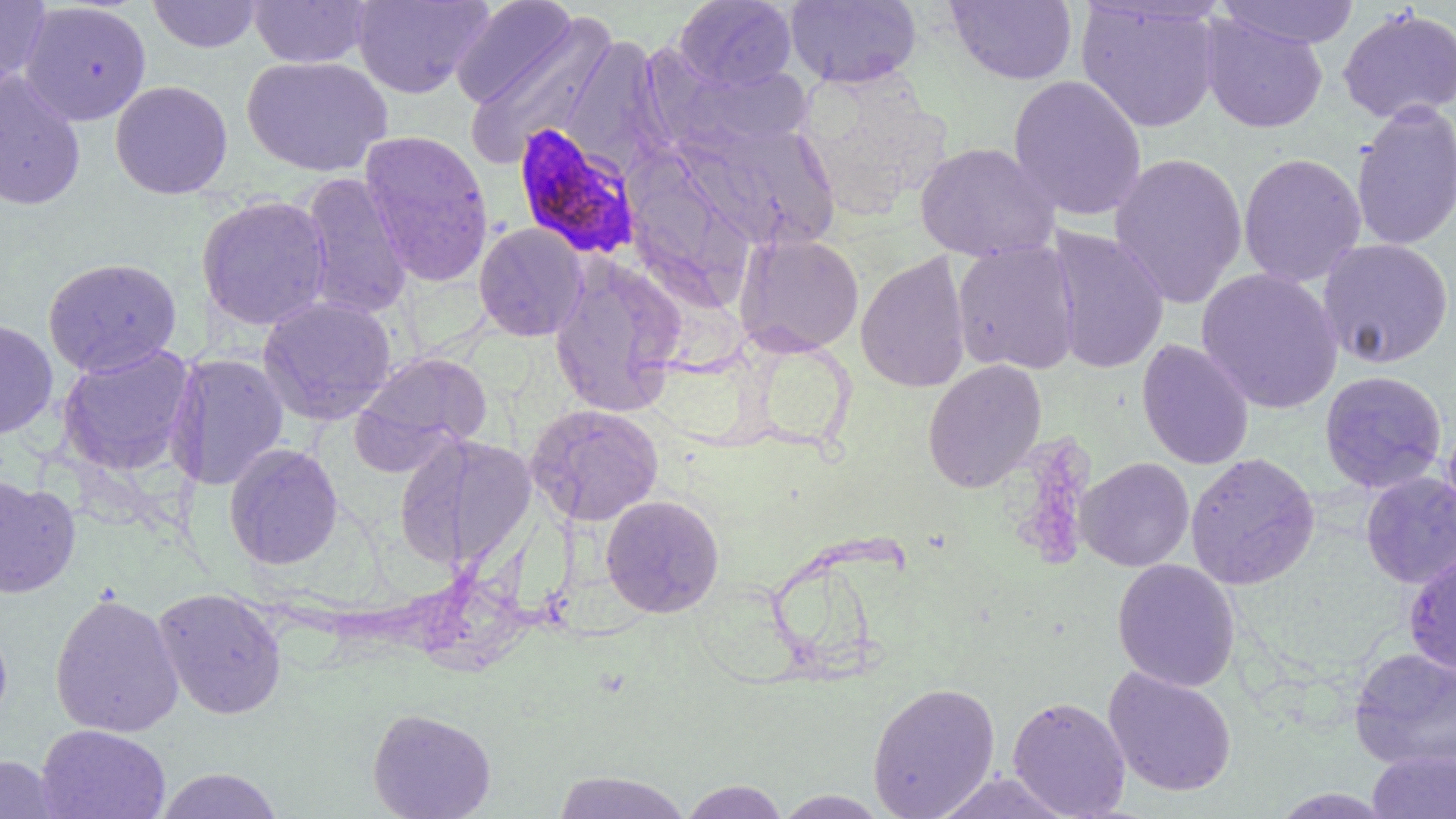

Summary:
  - Coordinate format: approximate bounding boxes as (x1,y1)-(x2,y2) corner pairs in pixels
  - Plasmodium falciparum-infected red blood cell locations (subset): (512,123)-(644,262)
  - Uninfected red blood cell locations (subset): (148,0)-(263,53), (248,0)-(373,68), (352,0)-(492,99), (450,0)-(579,110), (674,0)-(797,91), (785,0)-(921,88), (944,0)-(1078,85), (1216,0)-(1361,48), (0,1)-(51,87), (20,1)-(152,126), (1076,1)-(1222,133), (1337,6)-(1456,124), (462,12)-(619,169), (1200,12)-(1328,134), (562,34)-(673,176), (241,55)-(393,177), (679,62)-(815,151), (0,69)-(86,211), (795,69)-(951,219), (1008,74)-(1147,222), (110,79)-(233,199), (1351,101)-(1456,251), (673,118)-(841,251), (359,129)-(494,286), (914,141)-(1060,262), (622,146)-(757,311), (1109,152)-(1248,309), (1238,152)-(1367,287), (299,171)-(413,319), (195,194)-(332,331), (474,222)-(588,342), (1046,225)-(1170,374), (733,231)-(865,357), (1318,238)-(1454,369), (951,240)-(1080,375), (940,242)-(1064,494), (855,251)-(971,393), (43,257)-(182,377), (549,260)-(684,417), (1196,268)-(1343,414), (257,295)-(397,425), (0,318)-(58,438), (1137,339)-(1254,470), (56,344)-(196,476), (353,351)-(493,468), (165,353)-(289,490), (922,359)-(1047,493), (1319,370)-(1448,494), (526,403)-(665,526), (1442,414)-(1456,534), (394,433)-(536,571), (223,442)-(343,570), (1185,451)-(1321,590), (1076,457)-(1194,572), (1360,471)-(1456,588), (0,474)-(81,598), (600,494)-(725,618), (1112,558)-(1240,692), (152,587)-(287,719), (50,591)-(184,738), (0,616)-(12,729), (1349,647)-(1456,769), (1102,666)-(1238,797), (867,680)-(1000,819), (1007,695)-(1132,818), (367,707)-(496,819), (37,724)-(170,819), (1367,749)-(1456,818), (0,755)-(61,819), (154,767)-(283,818), (550,770)-(692,818), (931,771)-(1077,818), (678,780)-(789,818), (771,790)-(891,818)
  - Slide-level diagnosis: Plasmodium falciparum
  - Modality: optical microscopy
  - Field of view: single
  - Magnification: 1000x
  - Preparation: thin blood film
  - Image size: 1456×819 pixels